Classify this cell by malaria status.
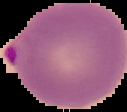

Parasitized.

Segmented cell region on a black background. From a thin blood film. Image is 127×112 pixels.